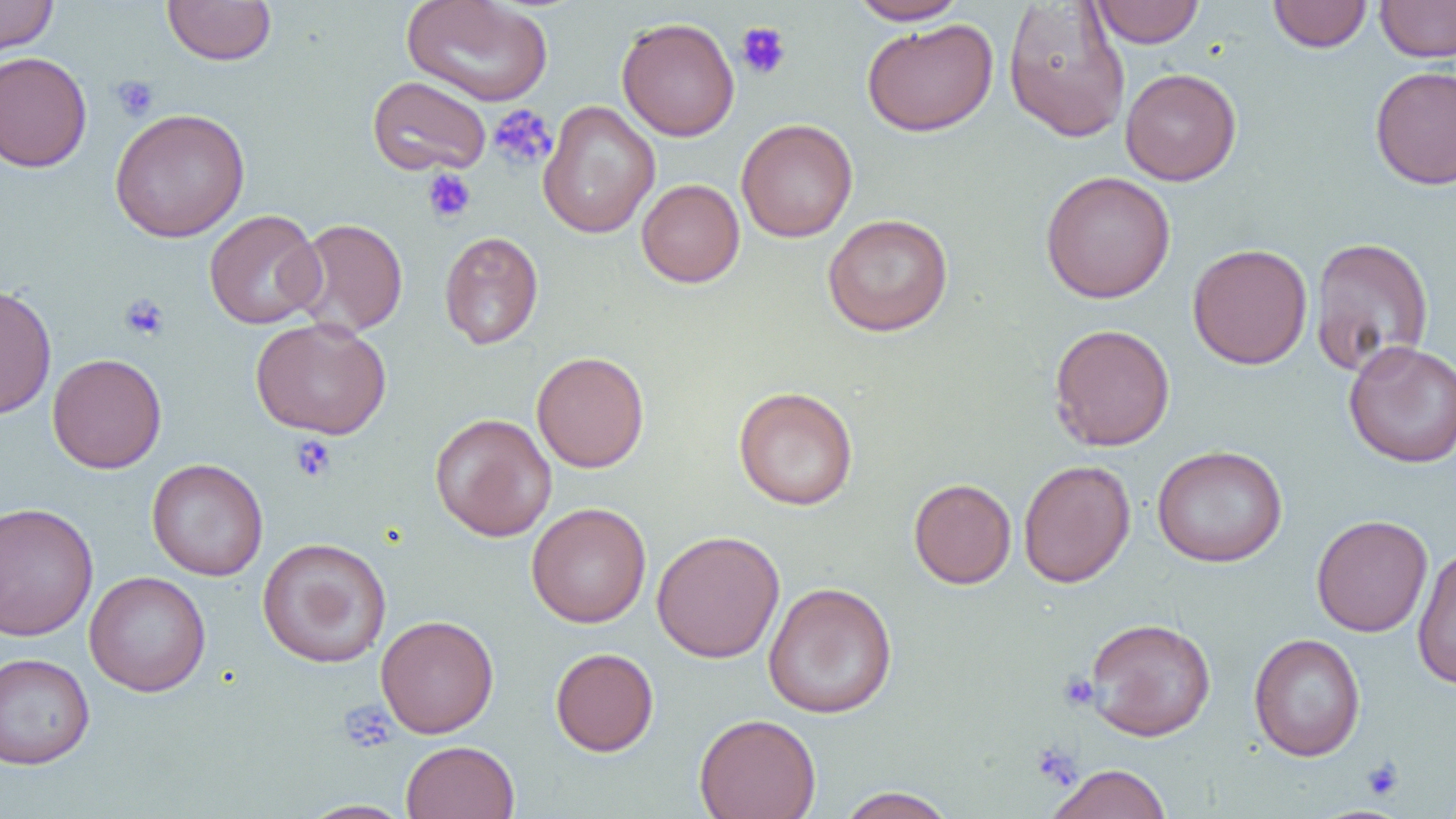

Summary:
  - Coordinate format: approximate bounding boxes as (x1,y1)-(x2,y2) corner pairs in pixels
  - Uninfected red blood cell locations: (0,0)-(58,57), (162,0)-(277,66), (401,0)-(553,106), (846,0)-(969,25), (1091,0)-(1204,47), (1267,0)-(1373,53), (1375,0)-(1456,62), (1002,2)-(1131,143), (616,17)-(740,142), (861,18)-(999,136), (0,51)-(92,172), (1370,65)-(1456,190), (1120,68)-(1242,186), (367,75)-(492,176), (538,100)-(660,239), (109,108)-(250,243), (736,119)-(858,243), (1039,170)-(1176,304), (636,179)-(745,288), (204,209)-(325,330), (822,213)-(954,336), (291,218)-(408,337), (439,230)-(543,349), (1309,236)-(1434,377), (1187,243)-(1313,369), (1,283)-(57,420), (249,317)-(392,440), (1048,323)-(1176,452), (1343,339)-(1456,469), (532,351)-(649,473), (46,353)-(167,473), (733,386)-(859,510), (430,413)-(557,541), (1151,445)-(1288,568), (146,458)-(268,581), (1018,460)-(1136,587), (909,478)-(1016,589), (1,502)-(98,641), (526,502)-(652,628), (1311,514)-(1433,637), (651,530)-(785,663), (257,537)-(392,668), (1412,546)-(1456,690), (85,571)-(211,696), (762,581)-(898,719), (376,614)-(499,738), (1084,617)-(1216,741), (1249,632)-(1366,761), (550,647)-(659,756), (0,653)-(95,769), (694,713)-(821,819), (401,740)-(519,819), (1046,763)-(1172,819), (1439,782)-(1456,819), (835,787)-(956,818), (298,799)-(413,818)
  - Platelet locations: (735,22)-(792,80), (111,75)-(160,122), (487,104)-(557,171), (422,168)-(476,224), (119,293)-(170,342), (290,434)-(337,482), (1058,671)-(1100,711), (340,700)-(397,753), (1031,743)-(1082,789), (1361,757)-(1404,800)
  - Slide-level diagnosis: negative for blood parasites
  - Magnification: 1000x
  - Image size: 1456×819 pixels
  - Modality: light microscopy
  - Preparation: thin blood smear
  - Field of view: single